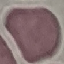
Summary:
  - Malaria status: uninfected
  - Preparation: thin blood smear
  - Stain: Giemsa
  - Capture: smartphone through the microscope eyepiece
  - Image type: cell patch, automatically extracted from a larger field of view and resized to 64 × 64 pixels